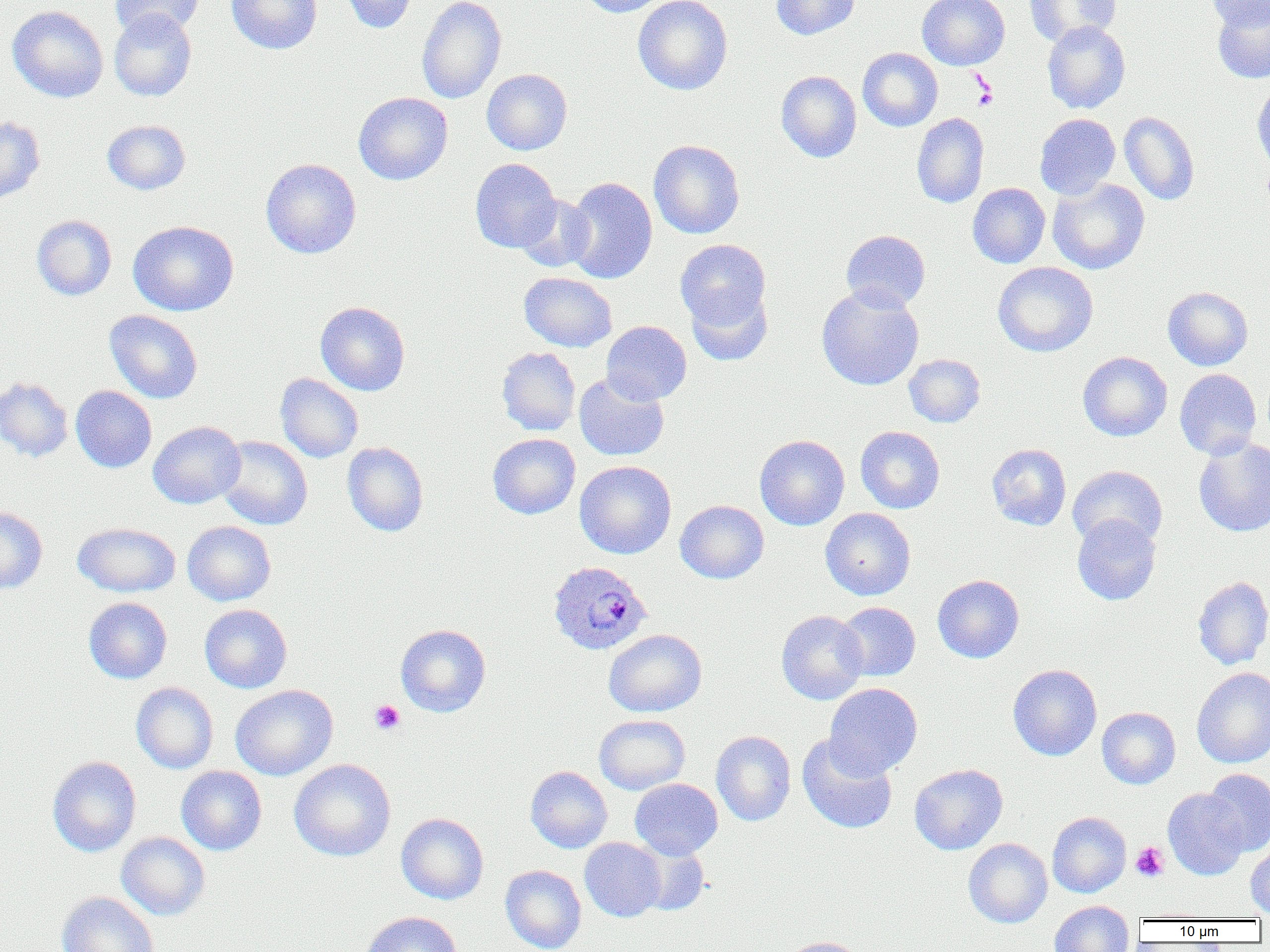 Approximate bounding boxes as named x1/y1/x2/y2 corners in pixels. Uninfected red blood cell locations: (x1=109, y1=0, x2=204, y2=39), (x1=226, y1=0, x2=322, y2=54), (x1=339, y1=0, x2=418, y2=34), (x1=417, y1=0, x2=506, y2=104), (x1=579, y1=0, x2=671, y2=17), (x1=633, y1=0, x2=733, y2=95), (x1=771, y1=0, x2=860, y2=40), (x1=917, y1=0, x2=1010, y2=70), (x1=1025, y1=0, x2=1120, y2=46), (x1=1207, y1=0, x2=1270, y2=30), (x1=1212, y1=2, x2=1270, y2=83), (x1=7, y1=5, x2=109, y2=103), (x1=109, y1=9, x2=197, y2=101), (x1=1042, y1=21, x2=1130, y2=113), (x1=858, y1=47, x2=942, y2=131), (x1=482, y1=69, x2=572, y2=155), (x1=776, y1=70, x2=861, y2=162), (x1=1251, y1=83, x2=1270, y2=174), (x1=353, y1=91, x2=453, y2=185), (x1=1119, y1=111, x2=1200, y2=205), (x1=912, y1=113, x2=989, y2=208), (x1=1034, y1=114, x2=1120, y2=199), (x1=0, y1=116, x2=45, y2=205), (x1=102, y1=120, x2=191, y2=195), (x1=648, y1=140, x2=745, y2=238), (x1=260, y1=158, x2=361, y2=259), (x1=470, y1=158, x2=561, y2=253), (x1=564, y1=177, x2=658, y2=284), (x1=1048, y1=178, x2=1150, y2=274), (x1=967, y1=183, x2=1050, y2=268), (x1=516, y1=194, x2=596, y2=273), (x1=32, y1=215, x2=117, y2=300), (x1=128, y1=220, x2=239, y2=316), (x1=841, y1=229, x2=931, y2=311), (x1=675, y1=239, x2=772, y2=332), (x1=993, y1=261, x2=1098, y2=357), (x1=519, y1=272, x2=617, y2=352), (x1=816, y1=285, x2=924, y2=391), (x1=685, y1=286, x2=773, y2=365), (x1=1163, y1=286, x2=1253, y2=370), (x1=315, y1=301, x2=410, y2=396), (x1=105, y1=309, x2=202, y2=404), (x1=601, y1=321, x2=691, y2=405), (x1=497, y1=347, x2=581, y2=436), (x1=1078, y1=351, x2=1172, y2=441), (x1=904, y1=354, x2=985, y2=427), (x1=1174, y1=368, x2=1262, y2=459), (x1=275, y1=373, x2=364, y2=462), (x1=574, y1=373, x2=670, y2=461), (x1=0, y1=377, x2=73, y2=462), (x1=70, y1=385, x2=156, y2=472), (x1=148, y1=421, x2=245, y2=509), (x1=855, y1=426, x2=945, y2=513), (x1=487, y1=433, x2=580, y2=519), (x1=215, y1=435, x2=313, y2=530), (x1=754, y1=435, x2=850, y2=530), (x1=1193, y1=437, x2=1270, y2=537), (x1=342, y1=442, x2=429, y2=536), (x1=987, y1=443, x2=1072, y2=530), (x1=575, y1=460, x2=676, y2=559), (x1=1067, y1=465, x2=1168, y2=551), (x1=675, y1=500, x2=769, y2=583), (x1=0, y1=507, x2=47, y2=593), (x1=820, y1=508, x2=915, y2=600), (x1=1072, y1=513, x2=1161, y2=606), (x1=182, y1=521, x2=276, y2=606), (x1=192, y1=521, x2=280, y2=694), (x1=72, y1=522, x2=181, y2=597), (x1=932, y1=575, x2=1024, y2=663), (x1=1192, y1=576, x2=1270, y2=669), (x1=83, y1=597, x2=172, y2=684), (x1=835, y1=602, x2=920, y2=682), (x1=200, y1=604, x2=292, y2=693), (x1=776, y1=610, x2=869, y2=704), (x1=395, y1=624, x2=491, y2=717), (x1=603, y1=629, x2=707, y2=717), (x1=1008, y1=664, x2=1102, y2=761), (x1=1192, y1=667, x2=1270, y2=768), (x1=131, y1=682, x2=218, y2=774), (x1=824, y1=683, x2=922, y2=779), (x1=230, y1=685, x2=338, y2=781), (x1=1097, y1=707, x2=1180, y2=789), (x1=594, y1=714, x2=690, y2=794), (x1=711, y1=731, x2=796, y2=826), (x1=797, y1=735, x2=898, y2=834), (x1=47, y1=756, x2=141, y2=857), (x1=289, y1=759, x2=396, y2=861), (x1=909, y1=763, x2=1008, y2=855), (x1=176, y1=766, x2=267, y2=855), (x1=526, y1=766, x2=612, y2=853), (x1=1203, y1=768, x2=1270, y2=855), (x1=630, y1=778, x2=723, y2=859), (x1=1162, y1=788, x2=1248, y2=880), (x1=1047, y1=811, x2=1131, y2=898), (x1=396, y1=813, x2=489, y2=904), (x1=116, y1=832, x2=210, y2=920), (x1=580, y1=837, x2=666, y2=921), (x1=963, y1=838, x2=1052, y2=928), (x1=631, y1=840, x2=710, y2=916), (x1=1246, y1=844, x2=1270, y2=917), (x1=501, y1=865, x2=587, y2=952), (x1=57, y1=891, x2=159, y2=952), (x1=1049, y1=900, x2=1135, y2=952), (x1=361, y1=911, x2=462, y2=952), (x1=780, y1=936, x2=866, y2=952). Plasmodium ovale-infected red blood cell locations: (x1=549, y1=561, x2=652, y2=655). Platelet locations: (x1=971, y1=74, x2=998, y2=111), (x1=369, y1=699, x2=405, y2=734), (x1=1131, y1=842, x2=1169, y2=881). Slide-level diagnosis: Plasmodium ovale. Image is 1270×952 pixels. Light microscopy. Thin blood film. 1000x magnification. Single field of view.